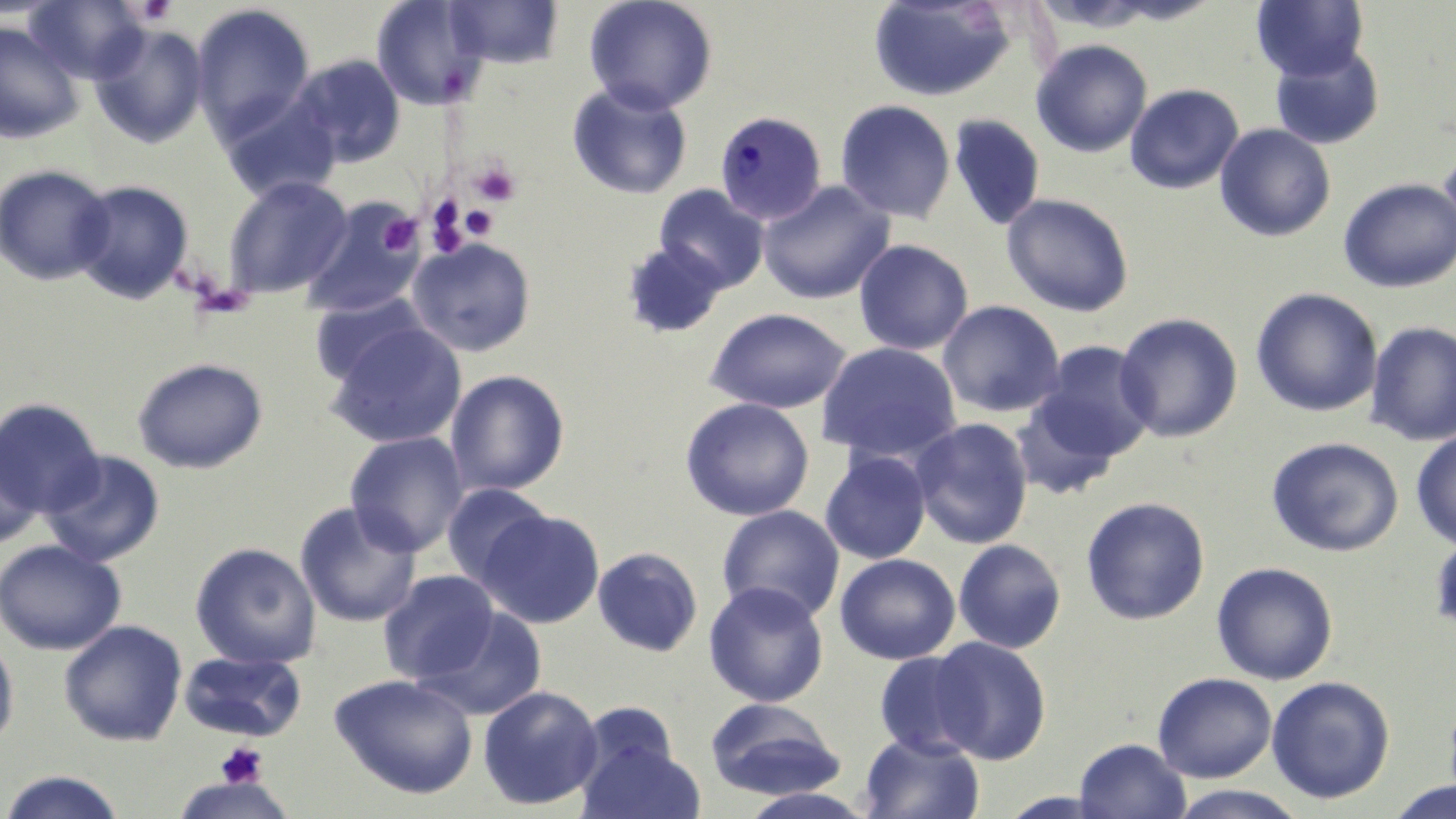

Summary:
  - Coordinate format: approximate bounding boxes as (x1, y1, x2, y2) in pixels
  - Platelet locations: (131, 0, 178, 26), (469, 158, 520, 206), (423, 199, 468, 254), (459, 205, 499, 240), (378, 214, 421, 255), (215, 742, 268, 789)
  - Plasmodium malariae-infected red blood cell locations: (714, 110, 827, 225)
  - Uninfected red blood cell locations: (24, 0, 150, 84), (371, 0, 488, 110), (444, 0, 564, 69), (583, 0, 718, 115), (868, 0, 1015, 102), (1104, 0, 1222, 25), (1252, 0, 1368, 82), (191, 3, 316, 144), (0, 22, 86, 143), (89, 22, 210, 148), (1030, 39, 1153, 158), (1270, 45, 1385, 149), (290, 54, 406, 167), (567, 82, 693, 200), (1124, 83, 1244, 194), (219, 95, 341, 204), (835, 99, 956, 224), (948, 113, 1045, 231), (1214, 123, 1337, 242), (1438, 149, 1456, 255), (0, 165, 115, 285), (223, 176, 353, 300), (1338, 177, 1456, 293), (70, 179, 194, 305), (758, 179, 895, 304), (653, 184, 770, 293), (1001, 193, 1135, 317), (300, 197, 428, 319), (407, 237, 536, 357), (854, 239, 974, 355), (621, 241, 728, 339), (1250, 287, 1383, 417), (309, 291, 434, 388), (937, 300, 1065, 418), (706, 307, 851, 414), (1114, 312, 1243, 442), (1365, 320, 1456, 445), (326, 323, 467, 448), (1032, 341, 1157, 463), (817, 342, 962, 465), (132, 357, 268, 474), (445, 369, 570, 496), (680, 396, 815, 521), (1011, 396, 1125, 499), (0, 398, 104, 518), (910, 418, 1033, 550), (1411, 430, 1456, 550), (344, 432, 469, 557), (0, 435, 45, 550), (1266, 436, 1404, 557), (41, 449, 166, 568), (820, 450, 931, 564), (441, 482, 554, 588), (1081, 496, 1210, 625), (294, 501, 421, 628), (717, 505, 844, 624), (478, 508, 605, 628), (1430, 532, 1456, 636), (953, 538, 1066, 653), (0, 539, 127, 655), (189, 542, 321, 669), (592, 546, 704, 657), (834, 553, 960, 665), (1211, 561, 1338, 685), (378, 570, 500, 686), (703, 581, 830, 707), (415, 606, 547, 722), (58, 620, 187, 747), (0, 631, 19, 750), (928, 637, 1051, 764), (178, 650, 307, 742), (874, 651, 985, 759), (1152, 672, 1277, 782), (329, 673, 478, 799), (1266, 676, 1395, 804), (477, 685, 603, 810), (704, 698, 845, 800), (858, 732, 985, 819), (576, 734, 705, 819), (1073, 737, 1191, 819), (0, 770, 130, 818), (170, 775, 297, 818), (1384, 780, 1456, 819), (1165, 785, 1312, 819), (736, 787, 878, 819)
  - Slide-level diagnosis: Plasmodium malariae
  - Image size: 1456×819 pixels
  - Field of view: one of a larger specimen
  - Preparation: thin blood smear
  - Stain: May-Grünwald-Giemsa
  - Magnification: 1000x
  - Modality: light microscopy